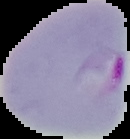

Malaria status: parasitized. Image is 130×139 pixels. Segmented cell region on a black background. From a thin blood smear.